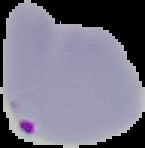

Summary:
  - Preparation: thin blood film
  - Image type: segmented cell region with the area outside set to black
  - Image size: 145×148 pixels
  - Result: malaria parasites identified